Classify this cell by malaria status.
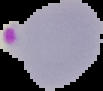
It is parasitized.

image type = segmented cell region on a black background
preparation = thin blood smear
image size = 103×91 pixels